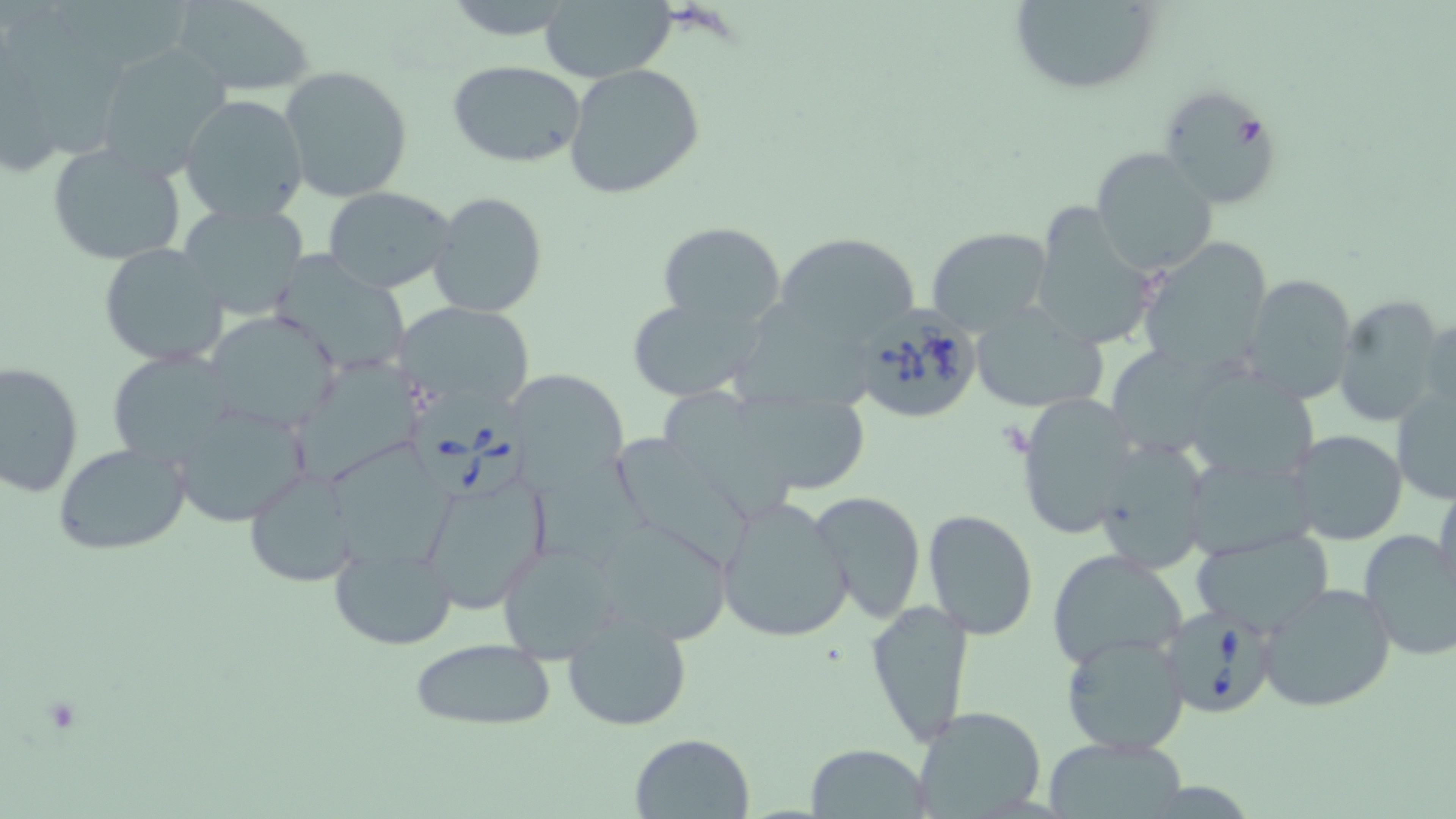
slide-level diagnosis = Babesia divergens
uninfected red blood cell locations = approximate bounding boxes as named x1/y1/x2/y2 corners in pixels: (x1=172, y1=0, x2=317, y2=95), (x1=537, y1=0, x2=678, y2=82), (x1=1004, y1=0, x2=1162, y2=95), (x1=53, y1=8, x2=189, y2=70), (x1=7, y1=15, x2=121, y2=163), (x1=94, y1=40, x2=236, y2=180), (x1=446, y1=60, x2=591, y2=166), (x1=563, y1=63, x2=705, y2=198), (x1=279, y1=64, x2=412, y2=202), (x1=1158, y1=83, x2=1278, y2=208), (x1=178, y1=93, x2=309, y2=225), (x1=46, y1=142, x2=188, y2=267), (x1=1090, y1=147, x2=1220, y2=278), (x1=321, y1=185, x2=457, y2=294), (x1=428, y1=190, x2=547, y2=319), (x1=1026, y1=201, x2=1163, y2=349), (x1=174, y1=202, x2=313, y2=321), (x1=654, y1=220, x2=787, y2=326), (x1=926, y1=227, x2=1054, y2=337), (x1=775, y1=229, x2=923, y2=346), (x1=1137, y1=236, x2=1274, y2=371), (x1=98, y1=242, x2=230, y2=367), (x1=265, y1=252, x2=415, y2=376), (x1=1241, y1=273, x2=1358, y2=406), (x1=1332, y1=294, x2=1450, y2=427), (x1=624, y1=295, x2=773, y2=404), (x1=393, y1=301, x2=538, y2=412), (x1=968, y1=304, x2=1106, y2=416), (x1=734, y1=305, x2=873, y2=412), (x1=204, y1=311, x2=342, y2=435), (x1=1107, y1=347, x2=1248, y2=452), (x1=106, y1=349, x2=241, y2=466), (x1=0, y1=358, x2=83, y2=498), (x1=278, y1=360, x2=422, y2=485), (x1=1184, y1=364, x2=1324, y2=486), (x1=507, y1=368, x2=629, y2=494), (x1=659, y1=385, x2=795, y2=523), (x1=1390, y1=385, x2=1456, y2=504), (x1=730, y1=392, x2=872, y2=492), (x1=1016, y1=394, x2=1142, y2=539), (x1=171, y1=403, x2=312, y2=526), (x1=1285, y1=431, x2=1408, y2=547), (x1=604, y1=435, x2=762, y2=572), (x1=1092, y1=437, x2=1214, y2=576), (x1=53, y1=443, x2=191, y2=555), (x1=330, y1=443, x2=462, y2=585), (x1=531, y1=459, x2=659, y2=573), (x1=416, y1=468, x2=553, y2=616), (x1=244, y1=469, x2=361, y2=588), (x1=1434, y1=482, x2=1456, y2=603), (x1=807, y1=491, x2=928, y2=623), (x1=715, y1=494, x2=855, y2=645), (x1=921, y1=509, x2=1040, y2=640), (x1=592, y1=515, x2=732, y2=644), (x1=1189, y1=527, x2=1335, y2=637), (x1=1357, y1=529, x2=1456, y2=664), (x1=494, y1=541, x2=622, y2=664), (x1=327, y1=543, x2=457, y2=650), (x1=1046, y1=548, x2=1188, y2=670), (x1=1258, y1=582, x2=1398, y2=713), (x1=865, y1=600, x2=975, y2=745), (x1=561, y1=612, x2=694, y2=731), (x1=1059, y1=632, x2=1190, y2=754), (x1=410, y1=637, x2=556, y2=732), (x1=910, y1=706, x2=1048, y2=819), (x1=628, y1=731, x2=757, y2=819), (x1=1042, y1=733, x2=1188, y2=818), (x1=804, y1=742, x2=934, y2=818)
platelet locations = approximate bounding boxes as named x1/y1/x2/y2 corners in pixels: (x1=1228, y1=110, x2=1270, y2=157), (x1=997, y1=418, x2=1033, y2=459)
image size = 1456×819 pixels
stain = May-Grünwald-Giemsa
Babesia divergens-infected red blood cell locations = approximate bounding boxes as named x1/y1/x2/y2 corners in pixels: (x1=847, y1=304, x2=986, y2=424), (x1=406, y1=387, x2=534, y2=505), (x1=1158, y1=608, x2=1279, y2=720)
modality = light microscopy
field of view = single
preparation = thin blood film
magnification = 1000x